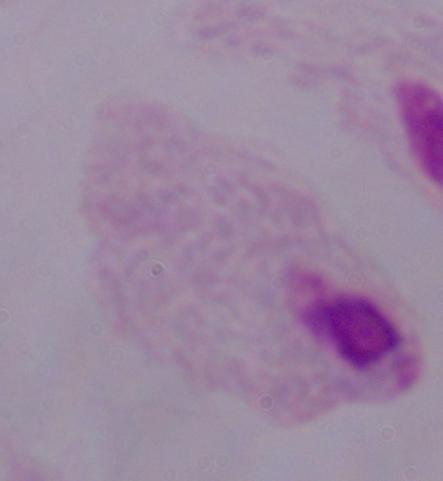

Summary:
  - Identification: trichomonad
  - Modality: micrograph
  - Magnification: 1000x